Give the position of every Plasmodium parasite visible.
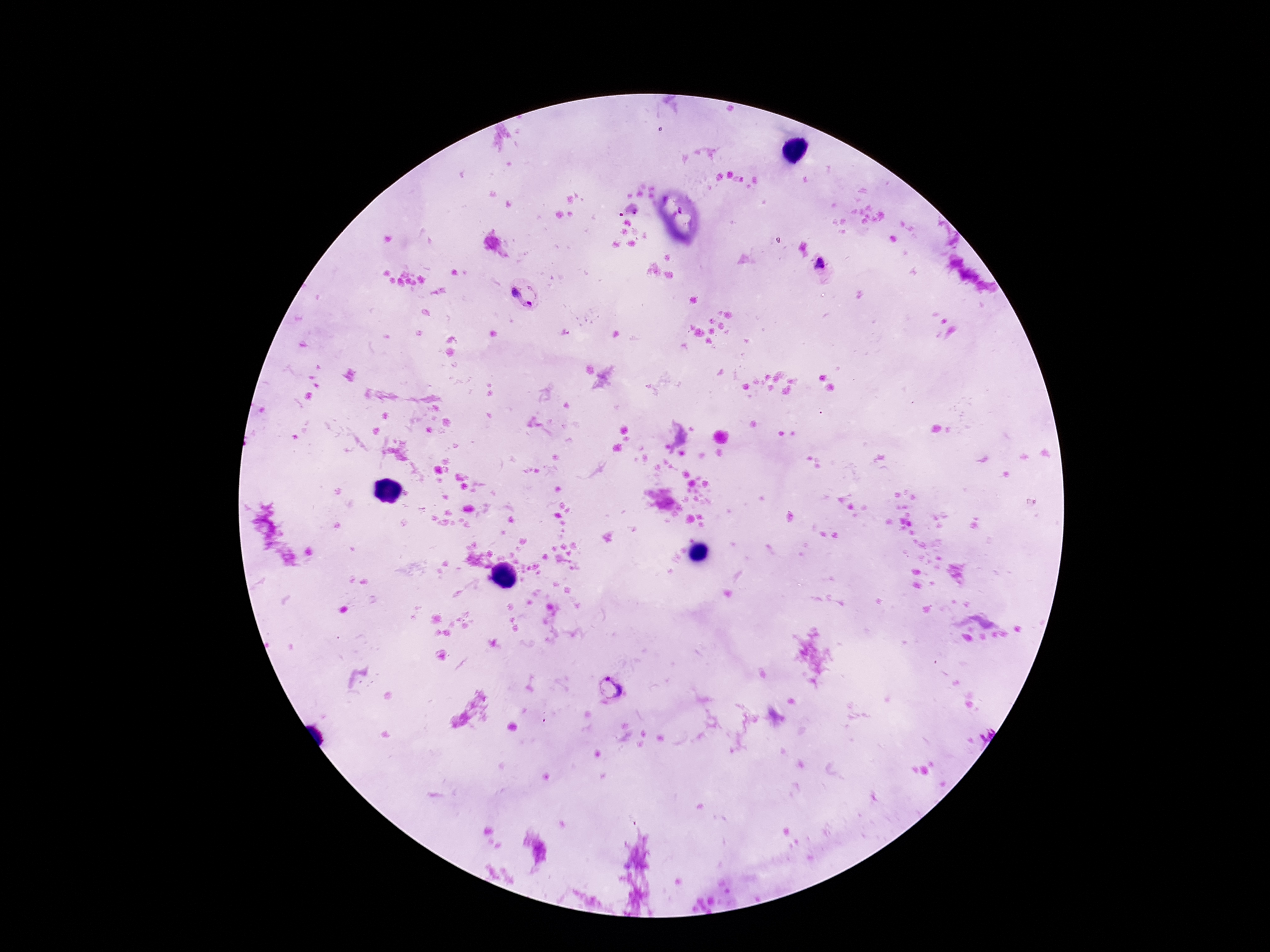
Approximate centers as {x, y} in pixels.
Plasmodium parasites: {821, 268}, {526, 294}, {612, 689}.

Patient malaria status: infected. Giemsa-stained preparation. 100x magnification. Image is 1270×952 pixels. Smartphone photograph taken through the microscope eyepiece. Single field of view. Thick peripheral-blood smear.